Locate every uninfected red blood cell.
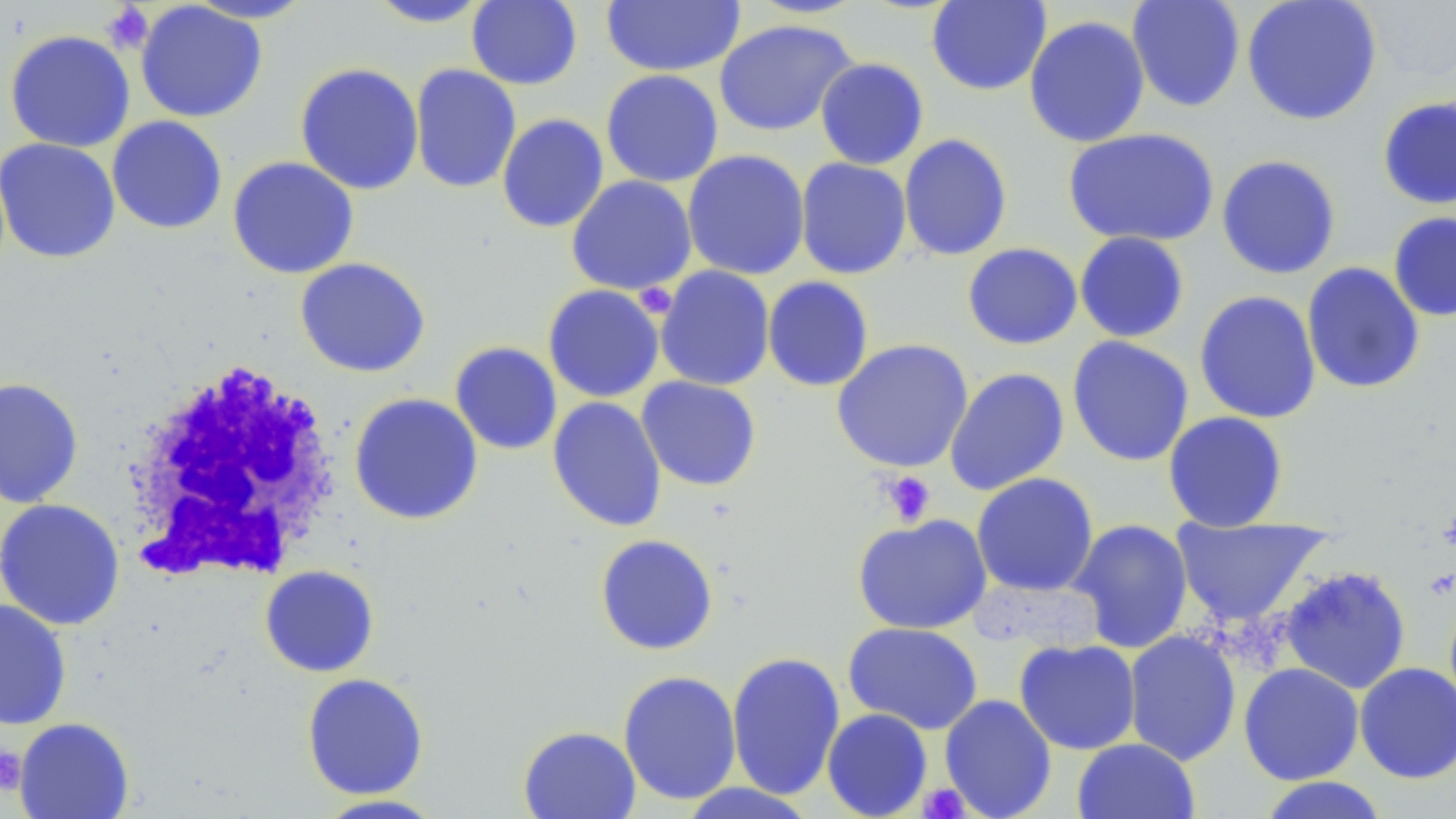
Approximate bounding boxes as [x1, y1, x2, y2] in pixels.
Uninfected red blood cells: [183, 0, 318, 24], [363, 0, 496, 28], [926, 0, 1052, 96], [1126, 0, 1246, 112], [1242, 0, 1382, 125], [466, 1, 583, 90], [601, 1, 745, 76], [135, 2, 267, 123], [1364, 2, 1456, 83], [1023, 15, 1150, 148], [714, 18, 858, 137], [4, 29, 136, 153], [814, 57, 929, 170], [294, 62, 424, 196], [409, 64, 521, 194], [600, 69, 724, 188], [1377, 96, 1456, 210], [496, 113, 609, 233], [106, 116, 228, 235], [1063, 127, 1219, 247], [898, 133, 1013, 261], [0, 138, 121, 264], [682, 149, 810, 280], [1216, 154, 1341, 279], [227, 156, 359, 279], [795, 157, 912, 279], [566, 175, 697, 295], [1388, 212, 1456, 322], [1074, 231, 1190, 343], [962, 242, 1083, 349], [295, 257, 430, 377], [1301, 262, 1425, 394], [655, 266, 775, 391], [762, 276, 874, 392], [542, 284, 665, 403], [1194, 290, 1321, 424], [1067, 336, 1195, 467], [831, 338, 973, 473], [450, 341, 562, 455], [944, 367, 1070, 496], [636, 376, 762, 491], [0, 377, 84, 508], [349, 393, 483, 525], [547, 396, 667, 532], [1162, 411, 1289, 532], [971, 472, 1099, 597], [0, 499, 125, 631], [852, 513, 992, 634], [1170, 517, 1331, 629], [1068, 518, 1194, 654], [595, 533, 719, 655], [259, 565, 379, 678], [1277, 565, 1412, 695], [0, 600, 72, 729], [843, 622, 984, 735], [1123, 630, 1241, 766], [1014, 638, 1141, 755], [726, 650, 846, 800], [1238, 662, 1364, 785], [1354, 662, 1456, 783], [617, 670, 742, 805], [301, 673, 429, 799], [939, 694, 1057, 819], [821, 708, 933, 819], [14, 717, 134, 819], [518, 725, 641, 819], [1072, 738, 1200, 819], [1256, 776, 1391, 819], [675, 782, 821, 818], [312, 794, 447, 818].

slide_level_diagnosis: negative for blood parasites
stain: May-Grünwald-Giemsa
modality: light microscopy
platelet_locations: 'approximate bounding boxes as [x1, y1, x2, y2] in pixels: [101, 3, 154, 54], [634, 283, 678, 319], [880, 470, 937, 526], [0, 747, 26, 794], [918, 783, 971, 818]'
magnification: 1000x
field_of_view: single
image_size: 1456×819 pixels
preparation: thin blood film
white_blood_cell_locations: 'approximate bounding boxes as [x1, y1, x2, y2] in pixels: [120, 359, 343, 583]'